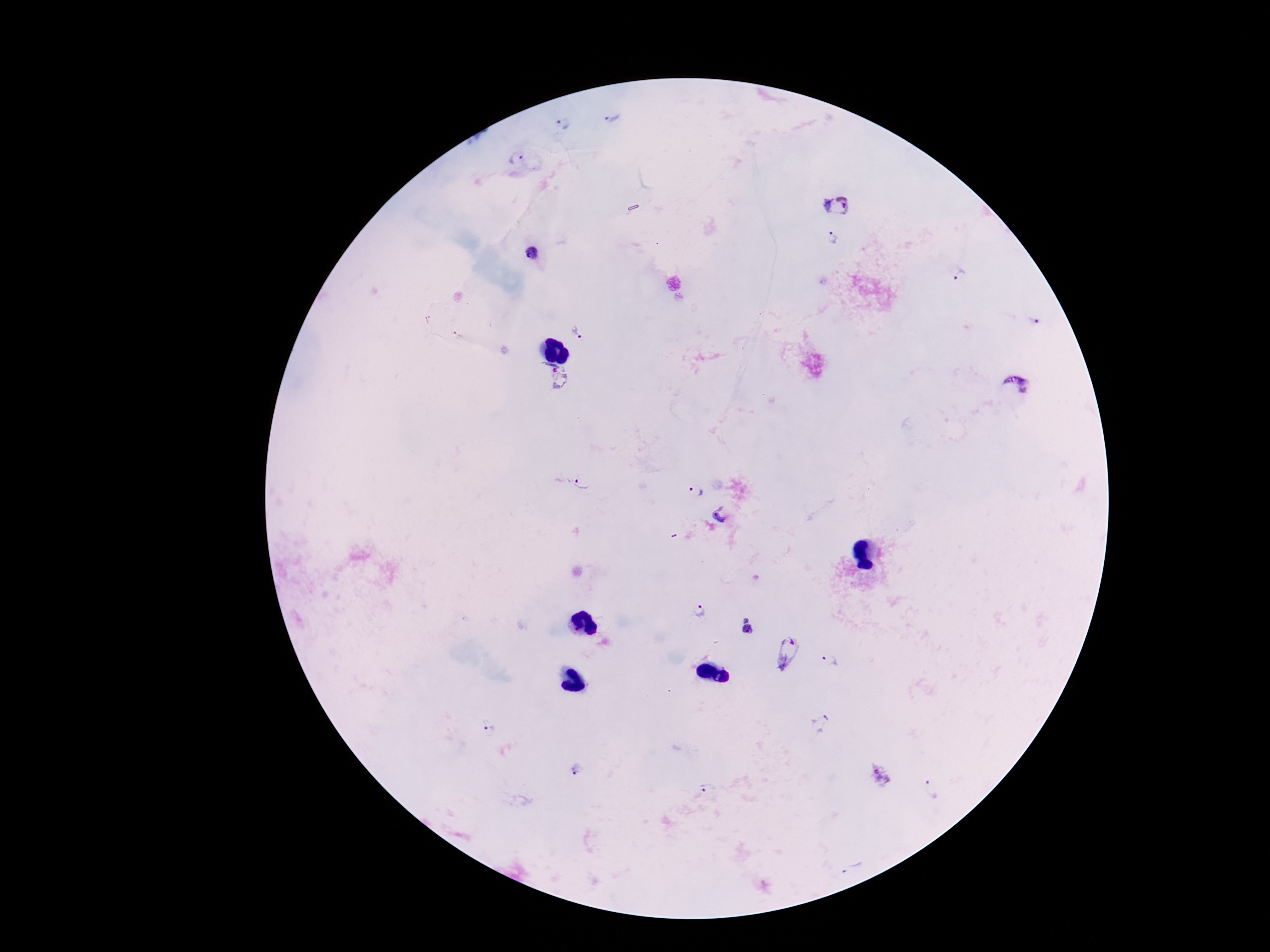
Approximate centers as [x, y] in pixels. Plasmodium parasite locations: [611, 117], [564, 124], [516, 157], [837, 205], [832, 239], [531, 252], [960, 274], [1033, 320], [578, 333], [555, 379], [1014, 389], [580, 483], [696, 490], [722, 515], [701, 610], [748, 627], [786, 653], [830, 662], [820, 722], [488, 728], [576, 769], [879, 775], [708, 788], [930, 788], [853, 866]. Giemsa-stained preparation. Single field of view. Image is 1270×952 pixels. Patient malaria status: infected. Photographed through the microscope eyepiece with a smartphone camera. Thick blood film. 100x magnification.